Report the malaria status of this cell.
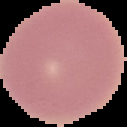
It is uninfected.

preparation = thin blood smear
image type = segmented cell region with the area outside set to black
image size = 127×127 pixels